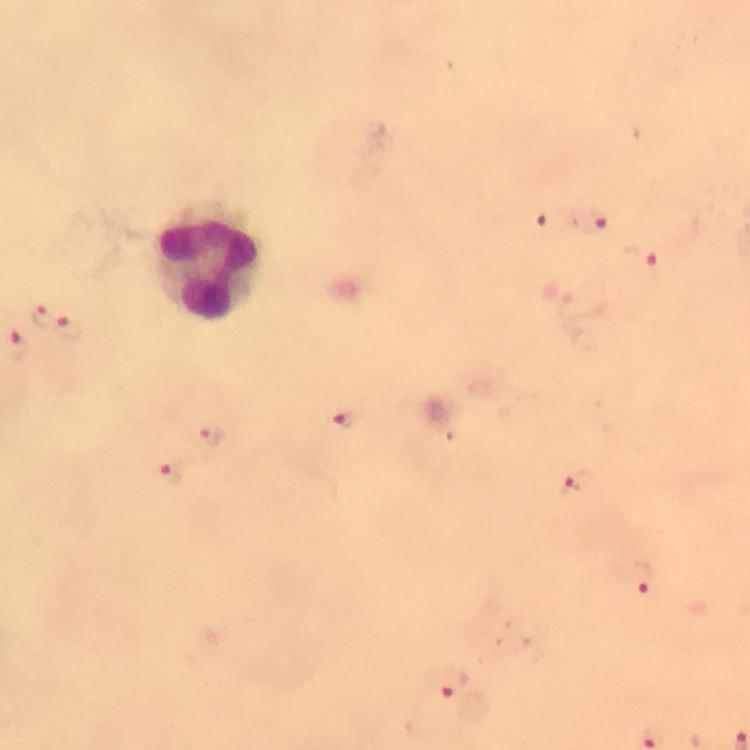

{
  "preparation": "thick blood film",
  "stain": "Giemsa",
  "malaria_parasite_locations": "approximate object centers, in pixels from the top-left corner: (x=546, y=222), (x=591, y=223), (x=641, y=259), (x=42, y=317), (x=68, y=329), (x=18, y=343), (x=344, y=420), (x=209, y=438), (x=169, y=473), (x=575, y=485), (x=643, y=576), (x=449, y=682)",
  "leukocyte_locations": "approximate object centers, in pixels from the top-left corner: (x=210, y=260)",
  "magnification": "100x",
  "capture": "smartphone camera through the microscope",
  "immersion_oil": "used",
  "context": "from a malaria diagnostic workup",
  "image_size": "750×750 pixels",
  "cropped_from": "a single field of view"
}